Comment on the morphology of the red blood cells.
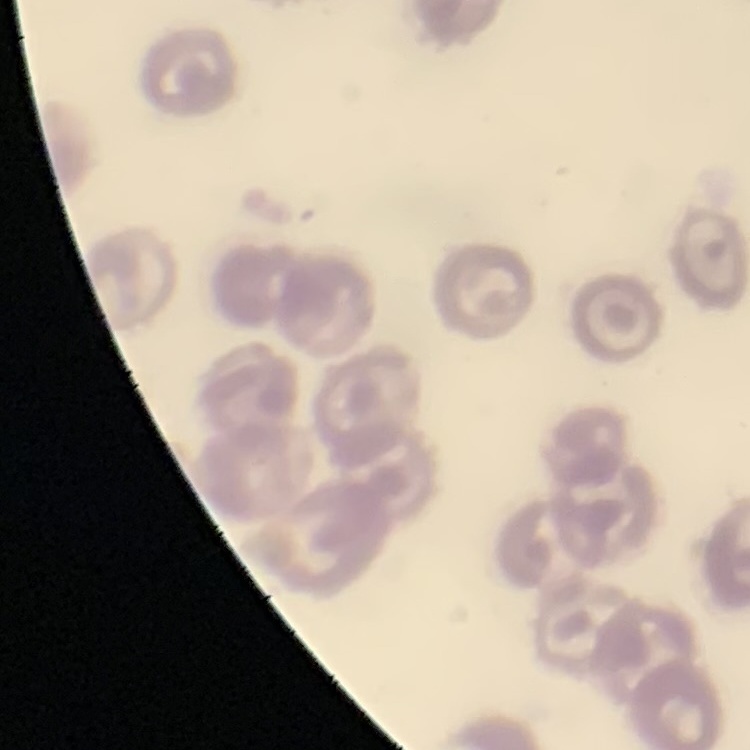
No rouleaux formation.

preparation: thin peripheral smear
image_type: square crop of a larger photomicrograph
stain: Field's or Giemsa